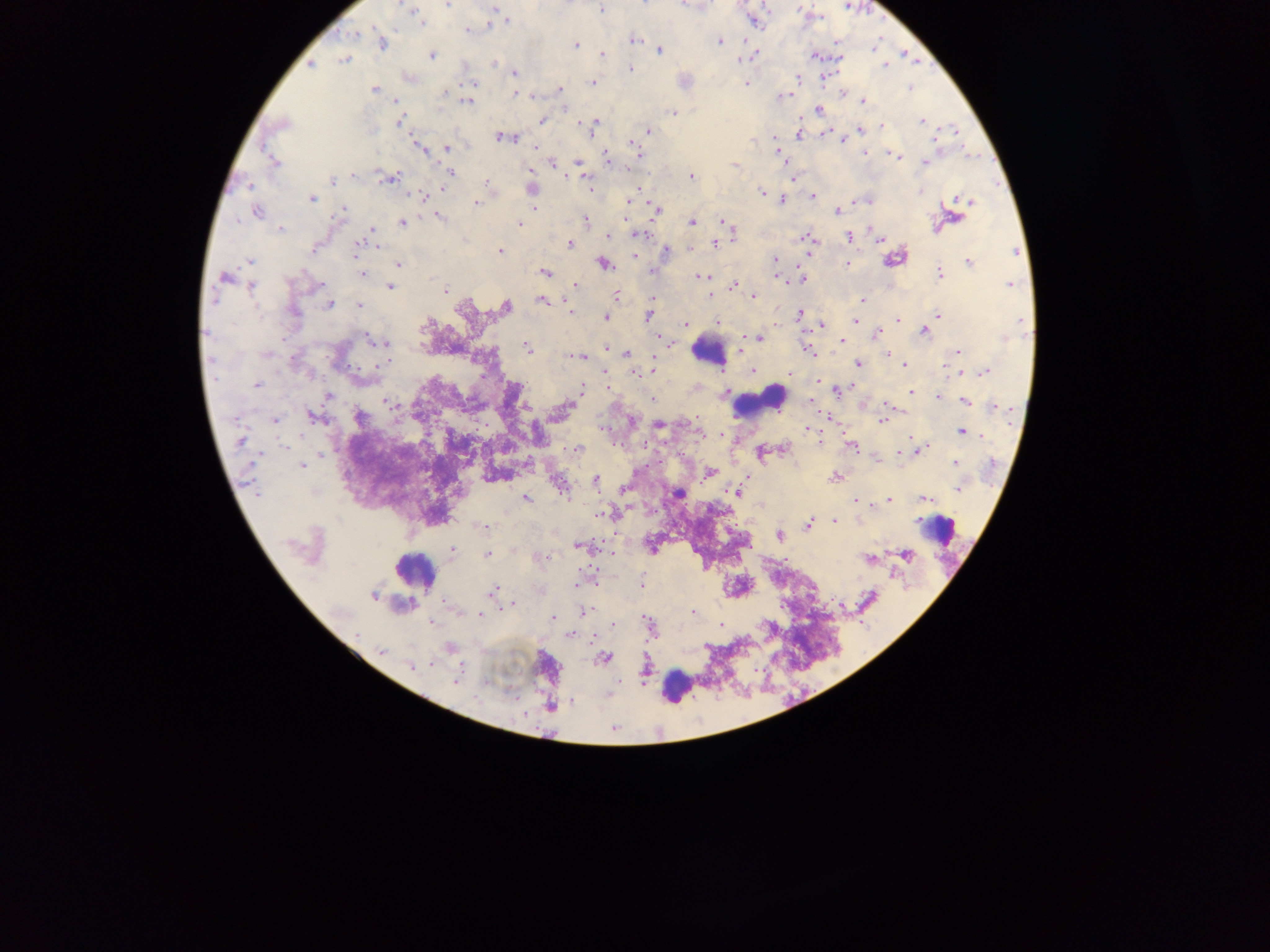

Approximate centers as x y in pixels.
Summary:
  - Leukocyte locations: 708 352; 761 402; 936 529; 415 570; 677 686
  - Plasmodium parasite locations: 447 5; 410 9; 601 9; 415 13; 418 18; 507 21; 469 31; 355 33; 634 40; 719 40; 382 43; 576 45; 659 50; 603 54; 431 55; 814 55; 344 59; 495 63; 311 65; 885 65; 631 69; 515 72; 798 78; 684 81; 471 83; 592 83; 746 83; 909 87; 374 89; 560 89; 517 95; 784 95; 396 101; 467 101; 864 101; 819 109; 672 112; 543 120; 400 121; 922 121; 596 122; 592 126; 883 126; 861 129; 648 132; 798 134; 502 137; 418 146; 448 148; 636 149; 777 152; 865 153; 894 156; 607 158; 273 162; 924 162; 578 163; 735 165; 580 169; 451 173; 353 175; 691 176; 388 177; 333 181; 486 183; 533 188; 762 192; 814 196; 422 197; 311 198; 782 199; 967 201; 628 202; 477 203; 535 206; 655 208; 257 211; 343 211; 838 211; 438 218; 585 220; 403 222; 691 222; 724 222; 518 224; 280 229; 730 229; 638 233; 609 236; 849 236; 880 237; 808 238; 361 244; 715 244; 570 245; 313 248; 666 249; 500 251; 635 256; 894 257; 775 260; 250 261; 969 262; 848 263; 399 264; 605 264; 653 271; 545 272; 363 273; 939 273; 224 277; 700 277; 802 280; 1009 284; 574 285; 734 285; 251 287; 390 287; 445 291; 712 293; 617 296; 753 296; 861 300; 543 301; 329 304; 359 306; 506 307; 570 309; 294 312; 800 314; 938 314; 648 316; 605 318; 854 319; 898 320; 717 321; 1021 323; 684 324; 823 325; 925 331; 878 333; 757 338; 372 339; 842 341; 380 342; 526 348; 609 348; 809 350; 958 350; 626 353; 888 354; 265 355; 574 356; 581 357; 294 361; 859 363; 654 364; 905 366; 752 371; 635 372; 985 372; 257 385; 581 389; 839 390; 911 392; 328 396; 939 397; 652 399; 966 401; 387 402; 994 407; 564 408; 314 417; 359 417; 882 420; 274 421; 659 425; 809 430; 963 432; 241 441; 852 446; 925 447; 577 449; 762 454; 900 454; 878 459; 955 462; 302 466; 710 473; 835 477; 596 482; 561 487; 624 489; 959 489; 736 492; 677 493; 526 498; 923 499; 856 501; 890 501; 606 514; 835 521; 809 525; 482 526; 780 535; 578 546; 452 549; 487 555; 907 555; 542 557; 868 558; 641 584; 493 591; 373 595; 868 599; 511 605; 585 611; 692 612; 480 616; 553 618; 648 623; 613 624; 720 625; 357 634; 569 635; 380 651; 604 658; 412 667; 456 680; 551 706
  - Image size: 1270×952 pixels
  - Capture: mobile-phone photograph through a microscope
  - Country: Ghana
  - Preparation: thick blood film
  - Field of view: single